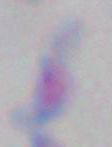 Toxoplasma gondii is shown. Captured at 1000x magnification. Photomicrograph.